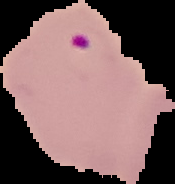
{
  "result": "Plasmodium parasites detected",
  "image_type": "segmented cell region on a black background",
  "preparation": "thin blood film",
  "image_size": "175×184 pixels"
}